Locate every Babesia divergens-infected red blood cell.
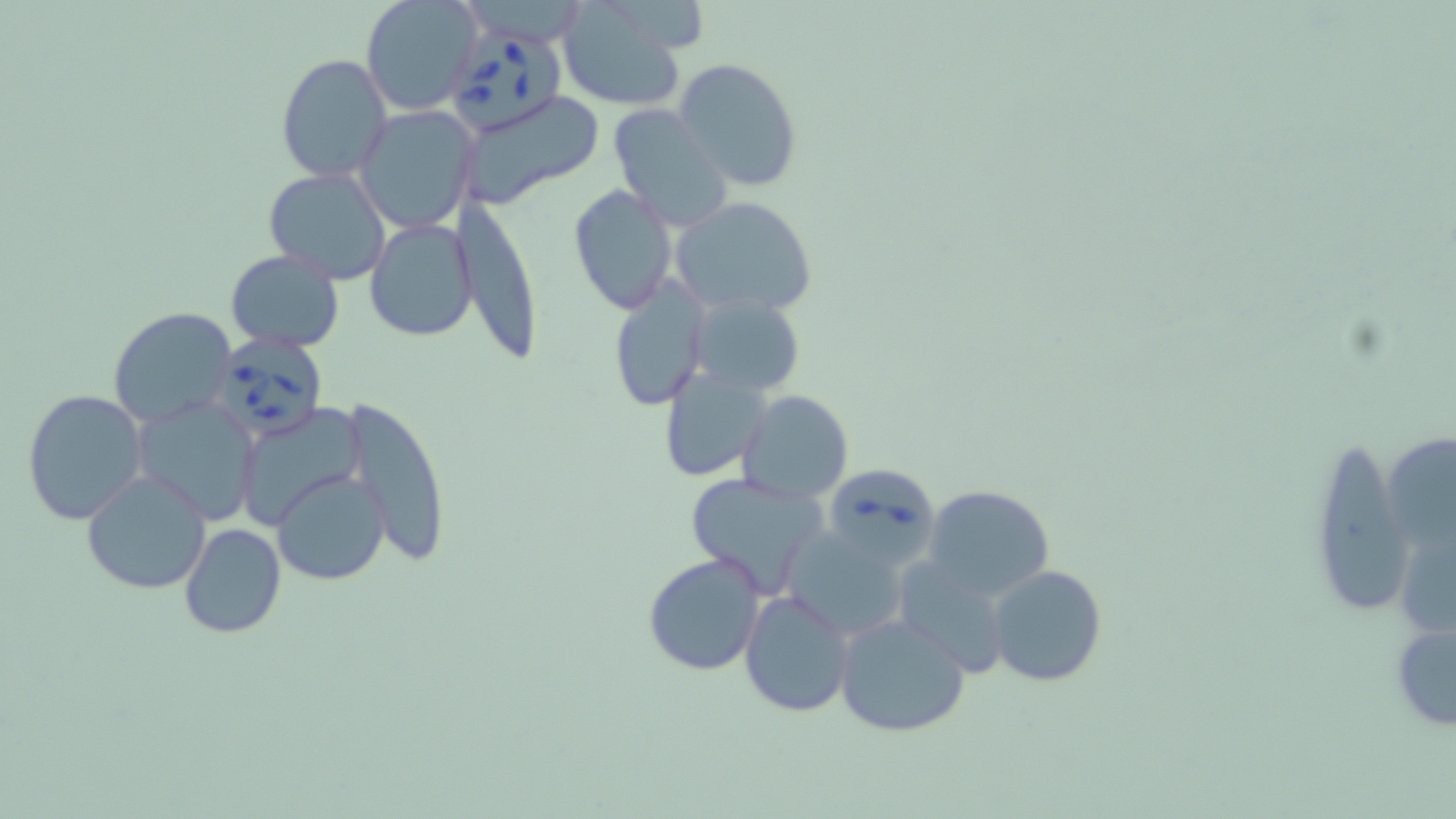

Approximate bounding boxes as [x1, y1, x2, y2] in pixels.
Babesia divergens-infected red blood cells: [445, 22, 568, 133], [208, 333, 328, 442], [820, 462, 941, 569].

Uninfected red blood cell locations: [360, 0, 482, 116], [555, 2, 692, 114], [276, 52, 394, 183], [674, 57, 803, 192], [458, 91, 601, 213], [607, 104, 731, 229], [355, 105, 480, 234], [263, 166, 392, 283], [569, 183, 678, 315], [452, 195, 544, 363], [670, 196, 819, 317], [364, 216, 479, 342], [225, 249, 344, 351], [608, 277, 709, 411], [687, 292, 808, 398], [107, 307, 236, 427], [656, 369, 772, 483], [21, 388, 147, 524], [736, 391, 854, 506], [130, 395, 261, 522], [341, 395, 452, 567], [235, 403, 368, 530], [1306, 433, 1414, 621], [272, 468, 390, 586], [80, 469, 212, 597], [683, 474, 828, 597], [923, 484, 1056, 603], [178, 523, 286, 638], [781, 525, 913, 640], [643, 553, 767, 676], [893, 555, 1018, 679], [987, 564, 1107, 687], [738, 588, 855, 719], [833, 612, 970, 739], [1390, 617, 1456, 733]. Slide-level diagnosis: Babesia divergens. May-Grünwald-Giemsa-stained preparation. Image is 1456×819 pixels. Thin blood smear. One field of a larger specimen. Captured at 1000x magnification. Light microscopy.